Assess the morphology of the red blood cells.
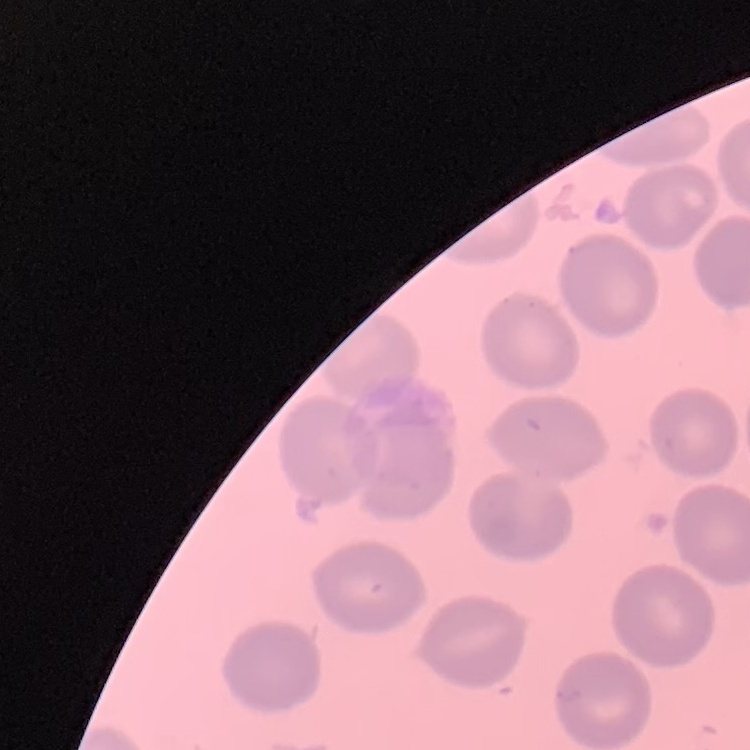
No rouleaux formation.

{
  "preparation": "thin blood smear",
  "image_type": "one tile cut from a larger photomicrograph",
  "stain": "Field's or Giemsa"
}